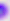

Summary:
  - Identification: Toxoplasma gondii
  - Modality: photomicrograph
  - Magnification: 400x